Assess this cell for malaria.
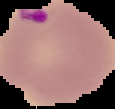
It is parasitized.

{
  "preparation": "thin blood smear",
  "image_size": "115×109 pixels",
  "image_type": "cell region segmented out of the field of view; surrounding area masked to black"
}